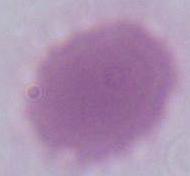
Summary:
  - Identification: red blood cell
  - Magnification: 1000x
  - Modality: photomicrograph